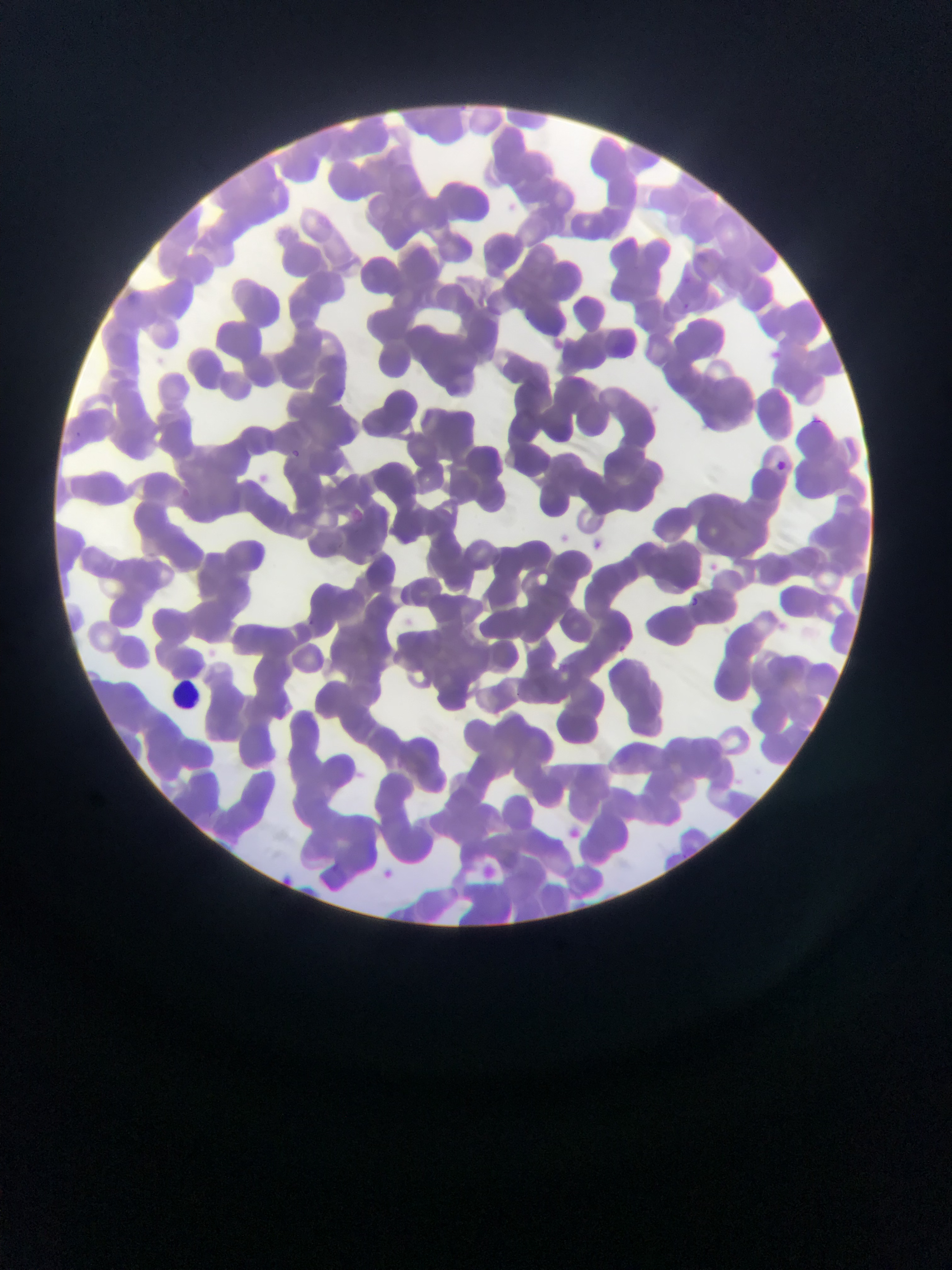

preparation = thin blood smear
leukocyte locations = approximate bounding boxes as {left, top, right, bottom} in pixels: {171, 676, 205, 709}
field of view = single
country = Ghana
image size = 952×1270 pixels
Plasmodium parasite locations = approximate bounding boxes as {left, top, right, bottom} in pixels: {813, 417, 824, 424}, {689, 596, 700, 607}
capture = mobile-phone photograph through a microscope